Name the cell type shown.
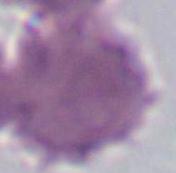

An erythrocyte.

Summary:
  - Magnification: 1000x
  - Modality: photomicrograph